Evaluate for parasitized red blood cells.
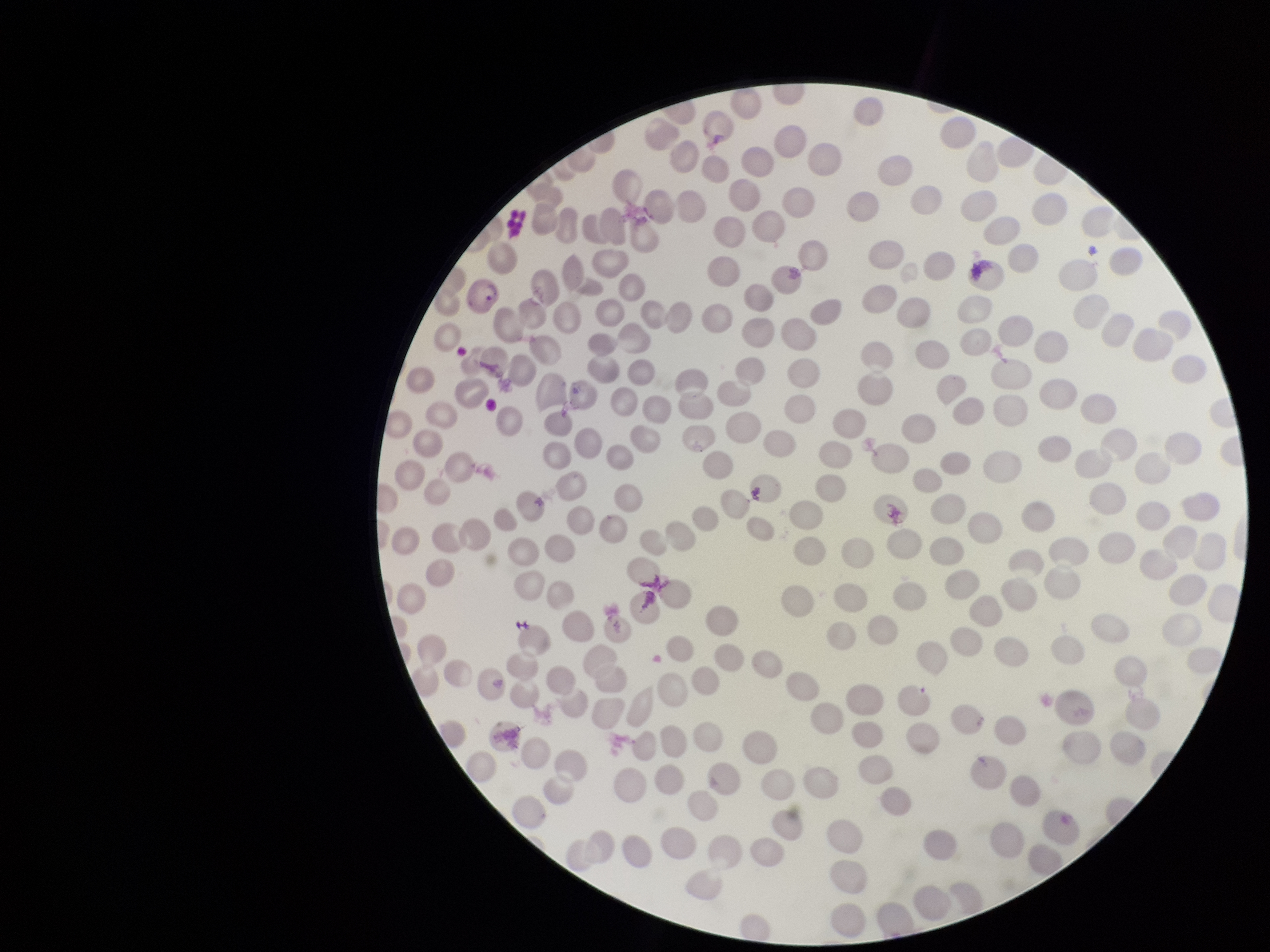
Identified.

Patient malaria status: positive. Preparation: thin smear. Parasitized red blood cell count: 1. Stained with Giemsa. Image is 1270×952 pixels. Species reported for this patient: Plasmodium vivax. Smartphone photograph taken through the eyepiece of a microscope. One field from this slide. Red blood cell count: 226.